Identify the blood parasite species.
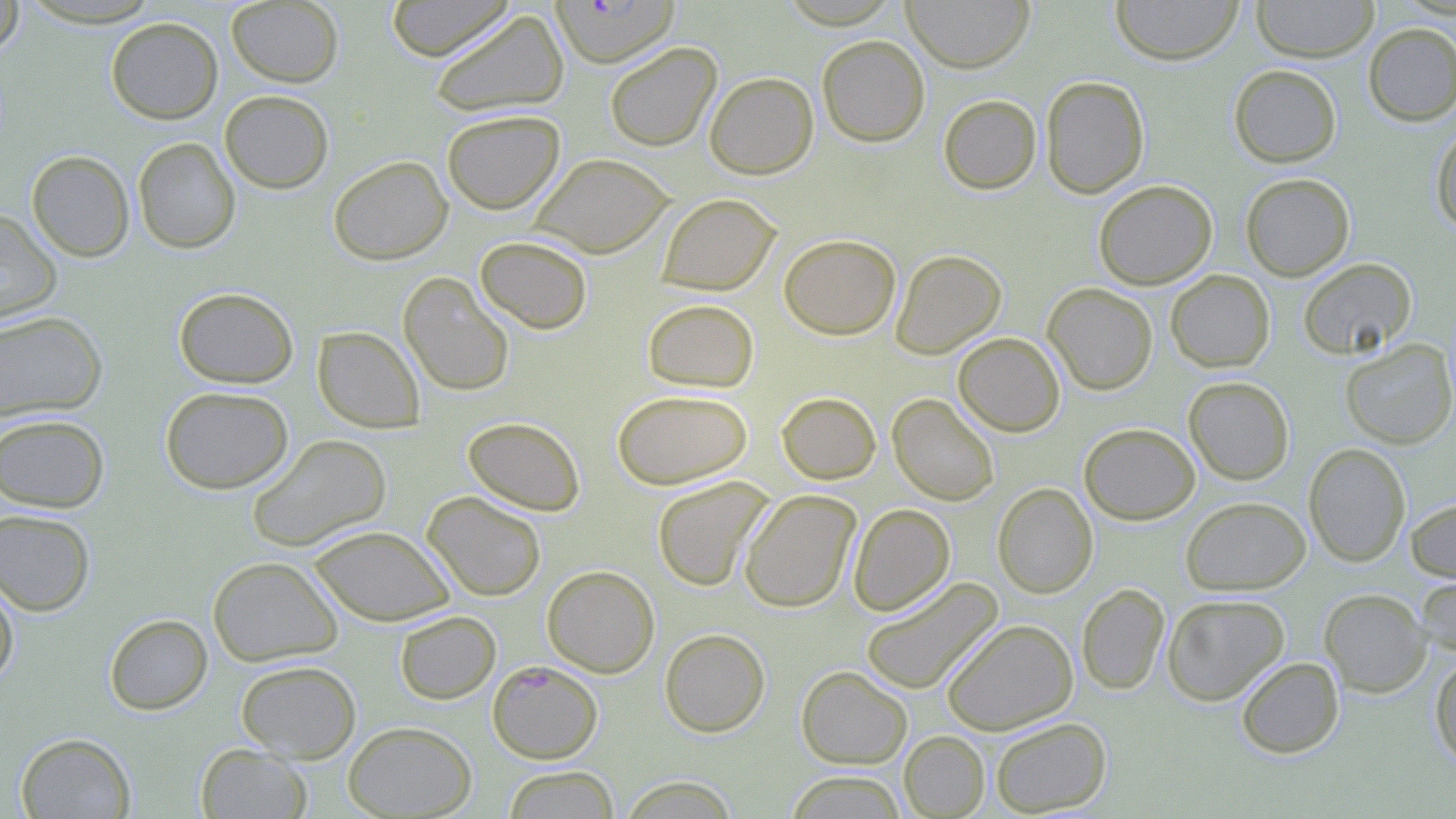

Plasmodium falciparum.

Approximate bounding boxes as named x1/y1/x2/y2 corners in pixels. Uninfected red blood cell locations: (x1=19, y1=0, x2=164, y2=28), (x1=226, y1=0, x2=344, y2=87), (x1=385, y1=0, x2=514, y2=61), (x1=902, y1=0, x2=1035, y2=73), (x1=1111, y1=0, x2=1244, y2=66), (x1=1251, y1=0, x2=1379, y2=63), (x1=0, y1=1, x2=24, y2=56), (x1=429, y1=9, x2=570, y2=118), (x1=106, y1=17, x2=223, y2=124), (x1=1362, y1=22, x2=1456, y2=126), (x1=816, y1=35, x2=930, y2=147), (x1=605, y1=42, x2=722, y2=152), (x1=1228, y1=64, x2=1342, y2=167), (x1=704, y1=71, x2=818, y2=179), (x1=1040, y1=75, x2=1149, y2=199), (x1=219, y1=90, x2=334, y2=193), (x1=938, y1=94, x2=1042, y2=194), (x1=442, y1=109, x2=566, y2=214), (x1=1430, y1=125, x2=1456, y2=233), (x1=132, y1=137, x2=240, y2=254), (x1=26, y1=150, x2=135, y2=262), (x1=530, y1=152, x2=675, y2=258), (x1=328, y1=155, x2=453, y2=265), (x1=1240, y1=172, x2=1355, y2=281), (x1=1093, y1=179, x2=1217, y2=289), (x1=657, y1=193, x2=781, y2=295), (x1=0, y1=209, x2=62, y2=327), (x1=778, y1=233, x2=901, y2=340), (x1=475, y1=236, x2=593, y2=334), (x1=890, y1=249, x2=1007, y2=359), (x1=1298, y1=258, x2=1416, y2=360), (x1=1166, y1=270, x2=1275, y2=372), (x1=398, y1=272, x2=515, y2=397), (x1=1042, y1=283, x2=1158, y2=395), (x1=173, y1=286, x2=299, y2=388), (x1=642, y1=298, x2=759, y2=393), (x1=0, y1=311, x2=108, y2=422), (x1=312, y1=326, x2=425, y2=432), (x1=953, y1=332, x2=1065, y2=437), (x1=1341, y1=339, x2=1456, y2=449), (x1=1183, y1=376, x2=1294, y2=485), (x1=160, y1=386, x2=293, y2=494), (x1=612, y1=389, x2=753, y2=489), (x1=776, y1=391, x2=881, y2=484), (x1=888, y1=394, x2=999, y2=506), (x1=0, y1=413, x2=110, y2=512), (x1=462, y1=416, x2=586, y2=516), (x1=1079, y1=423, x2=1200, y2=525), (x1=247, y1=434, x2=392, y2=552), (x1=1304, y1=443, x2=1411, y2=566), (x1=651, y1=476, x2=774, y2=591), (x1=992, y1=482, x2=1098, y2=598), (x1=739, y1=489, x2=861, y2=613), (x1=422, y1=491, x2=547, y2=601), (x1=1180, y1=496, x2=1311, y2=595), (x1=1405, y1=496, x2=1456, y2=582), (x1=848, y1=504, x2=955, y2=616), (x1=0, y1=508, x2=96, y2=616), (x1=308, y1=525, x2=455, y2=626), (x1=207, y1=556, x2=343, y2=667), (x1=542, y1=565, x2=659, y2=678), (x1=1416, y1=571, x2=1456, y2=658), (x1=860, y1=577, x2=1004, y2=696), (x1=0, y1=578, x2=19, y2=688), (x1=1077, y1=583, x2=1170, y2=695), (x1=1318, y1=588, x2=1431, y2=697), (x1=1162, y1=593, x2=1290, y2=706), (x1=394, y1=610, x2=501, y2=704), (x1=104, y1=613, x2=213, y2=715), (x1=942, y1=618, x2=1078, y2=735), (x1=660, y1=628, x2=770, y2=737), (x1=1429, y1=652, x2=1456, y2=768), (x1=1236, y1=656, x2=1344, y2=759), (x1=236, y1=659, x2=361, y2=762), (x1=796, y1=665, x2=912, y2=769), (x1=989, y1=717, x2=1112, y2=816), (x1=343, y1=720, x2=477, y2=818), (x1=899, y1=731, x2=989, y2=818), (x1=15, y1=732, x2=136, y2=818), (x1=196, y1=743, x2=312, y2=818), (x1=502, y1=765, x2=619, y2=818), (x1=784, y1=771, x2=908, y2=818), (x1=619, y1=775, x2=739, y2=818). Plasmodium falciparum-infected red blood cell locations: (x1=550, y1=0, x2=680, y2=68), (x1=487, y1=660, x2=603, y2=763). Optical microscopy. Captured at 1000x magnification. Thin blood film. Image is 1456×819 pixels. One field of a larger specimen. May-Grünwald-Giemsa-stained preparation.